Point out every malaria parasite.
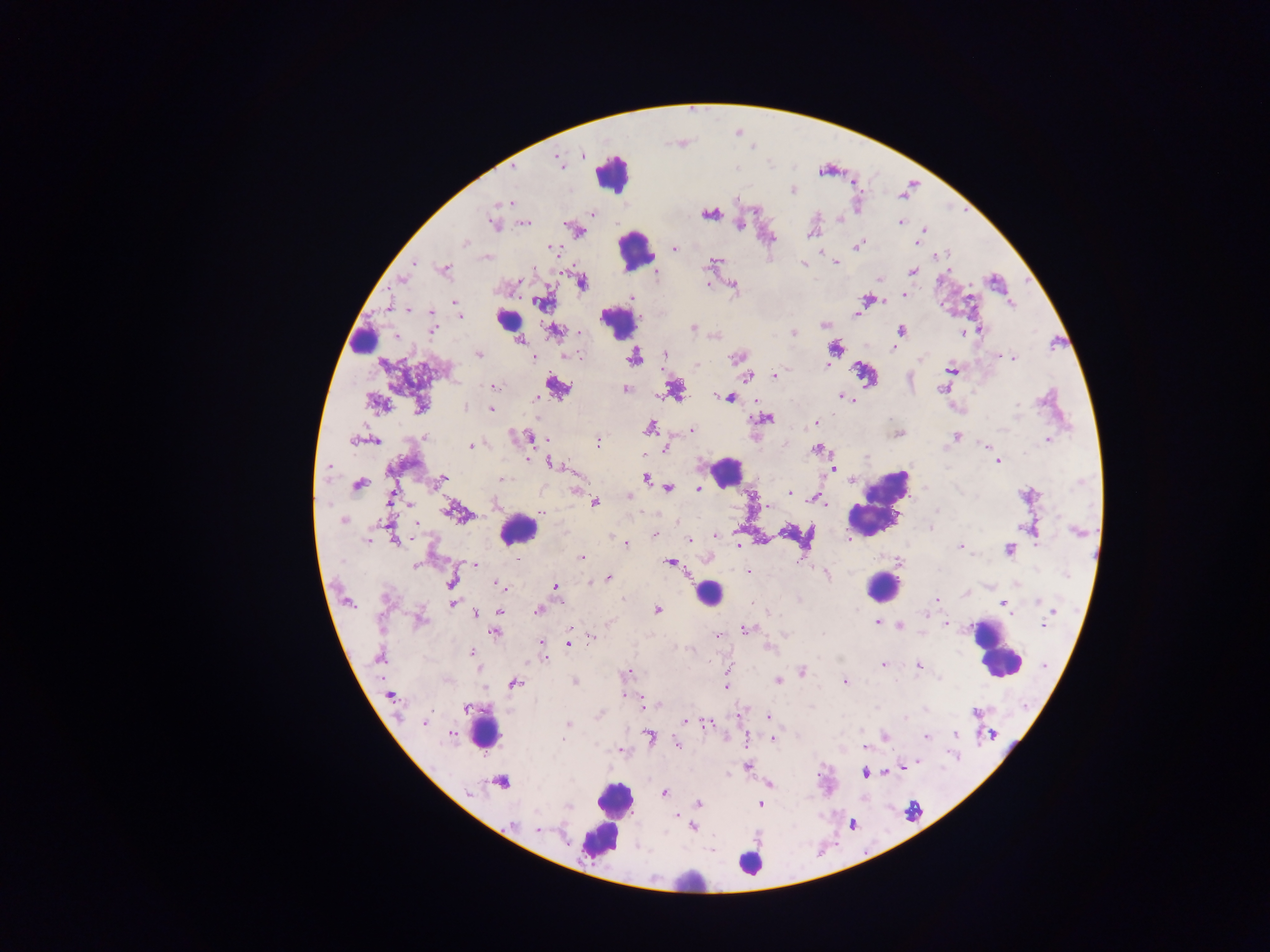
Approximate centers as x y in pixels.
Malaria parasites: 582 155; 559 161; 513 167; 792 190; 737 199; 497 203; 505 203; 592 213; 709 214; 839 217; 900 223; 493 224; 524 224; 739 224; 924 230; 810 233; 916 242; 464 243; 857 245; 553 247; 674 248; 821 253; 944 255; 938 256; 489 257; 713 261; 414 263; 835 263; 803 264; 533 269; 444 270; 913 271; 657 273; 402 278; 880 279; 582 282; 708 284; 733 287; 904 295; 632 298; 867 299; 455 302; 540 303; 1011 304; 409 310; 431 313; 856 314; 460 317; 824 325; 693 327; 433 330; 555 330; 902 330; 980 330; 580 333; 793 333; 963 333; 519 340; 835 348; 894 348; 479 354; 664 354; 568 355; 999 356; 534 357; 737 357; 634 358; 1013 358; 921 359; 697 365; 827 365; 951 369; 747 375; 775 375; 495 387; 557 388; 625 389; 942 389; 840 397; 730 398; 847 398; 537 399; 851 400; 375 403; 1017 405; 420 407; 465 407; 491 408; 766 418; 816 423; 650 428; 692 430; 1003 430; 898 433; 956 436; 425 437; 529 437; 353 440; 1048 440; 376 441; 598 442; 470 445; 986 446; 666 448; 818 450; 998 462; 551 464; 329 467; 833 469; 646 478; 853 478; 502 479; 441 480; 358 485; 669 489; 698 489; 577 492; 788 493; 793 495; 630 496; 390 498; 815 498; 595 502; 821 502; 409 504; 496 504; 767 506; 453 510; 937 511; 541 513; 344 521; 416 523; 1021 527; 931 528; 1077 532; 655 535; 714 536; 689 539; 368 540; 396 541; 625 543; 738 544; 960 546; 1009 550; 581 557; 670 563; 475 564; 415 566; 748 572; 827 574; 1067 575; 608 578; 452 583; 500 586; 555 587; 936 600; 1038 602; 453 604; 1004 604; 538 610; 657 610; 499 611; 1053 611; 478 613; 925 615; 420 620; 610 623; 877 623; 946 624; 1043 624; 497 626; 571 627; 901 627; 746 629; 495 633; 719 634; 823 634; 592 637; 542 643; 568 644; 769 649; 472 651; 378 657; 543 658; 883 665; 918 666; 802 671; 628 673; 778 680; 574 682; 844 682; 515 684; 726 686; 624 695; 390 696; 466 707; 975 713; 769 716; 905 718; 684 722; 425 723; 568 724; 707 724; 956 733; 453 734; 650 736; 885 737; 926 737; 772 738; 563 740; 678 745; 863 747; 916 763; 747 767; 903 767; 887 772; 864 773; 501 782; 768 784; 664 793; 470 794; 698 803; 761 804; 569 807; 676 815; 512 824; 693 826; 537 829; 712 850.

Summary:
  - Leukocyte locations: 613 172; 636 250; 508 320; 619 330; 362 342; 724 472; 877 503; 518 530; 882 587; 707 594; 995 649; 485 730; 612 812; 749 864; 688 881
  - Country: Ghana
  - Preparation: thick blood smear
  - Capture: mobile-phone photograph through a microscope
  - Field of view: single
  - Image size: 1270×952 pixels